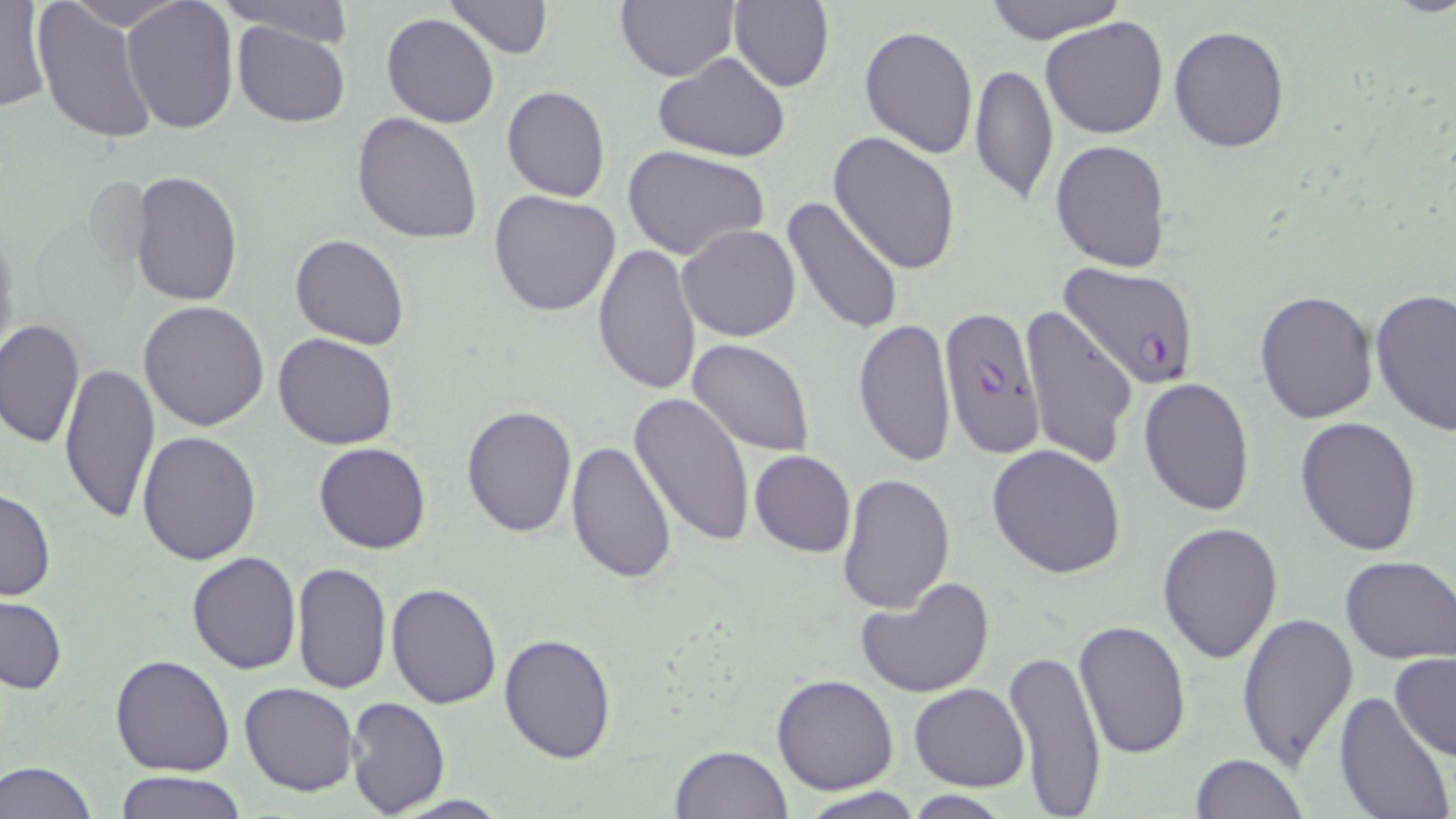
slide_level_diagnosis: Plasmodium falciparum
uninfected_red_blood_cell_locations: 'approximate bounding boxes as (x1, y1, x2, y2) in pixels: (64, 0, 185, 32), (219, 0, 354, 45), (443, 0, 554, 59), (979, 0, 1128, 44), (120, 1, 239, 134), (726, 1, 836, 90), (0, 2, 48, 113), (32, 2, 158, 144), (615, 2, 740, 80), (382, 13, 498, 128), (1040, 17, 1168, 139), (232, 22, 350, 128), (858, 26, 978, 159), (1168, 26, 1289, 153), (651, 52, 792, 162), (969, 63, 1058, 204), (501, 85, 610, 202), (353, 113, 482, 244), (829, 132, 961, 274), (1050, 139, 1174, 272), (621, 143, 769, 261), (130, 169, 242, 305), (489, 190, 621, 316), (783, 196, 908, 340), (676, 224, 801, 342), (0, 228, 20, 366), (290, 233, 410, 349), (593, 244, 702, 398), (1369, 288, 1456, 437), (1255, 290, 1377, 425), (139, 300, 270, 431), (1021, 305, 1137, 469), (1, 319, 84, 451), (853, 319, 956, 467), (273, 333, 398, 450), (688, 339, 816, 456), (57, 360, 160, 526), (1138, 376, 1255, 515), (628, 392, 756, 548), (461, 404, 577, 538), (1295, 417, 1424, 557), (137, 432, 261, 565), (567, 440, 677, 585), (314, 442, 431, 554), (988, 444, 1127, 579), (750, 450, 855, 558), (836, 472, 956, 616), (0, 487, 56, 602), (1156, 521, 1284, 664), (186, 552, 302, 674), (1340, 554, 1456, 666), (291, 562, 392, 695), (854, 575, 994, 698), (387, 582, 501, 709), (0, 596, 67, 696), (1237, 611, 1359, 773), (1075, 619, 1192, 762), (498, 631, 617, 763), (1003, 647, 1107, 814), (1389, 652, 1456, 763), (111, 653, 236, 775), (770, 674, 898, 795), (240, 682, 359, 798), (909, 683, 1029, 791), (1334, 692, 1453, 819), (344, 696, 450, 817), (668, 744, 793, 819), (1189, 753, 1309, 818), (0, 761, 98, 819), (114, 771, 248, 818), (798, 788, 928, 819), (902, 792, 1015, 818)'
modality: optical microscopy
magnification: 1000x
stain: May-Grünwald-Giemsa
preparation: thin blood film
plasmodium_falciparum_infected_red_blood_cell_locations: 'approximate bounding boxes as (x1, y1, x2, y2) in pixels: (1059, 260, 1201, 389), (938, 303, 1044, 459)'
image_size: 1456×819 pixels
field_of_view: single